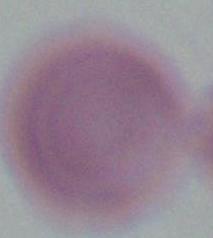
{
  "identification": "erythrocyte",
  "magnification": "1000x",
  "modality": "micrograph"
}